Assess the morphology of the erythrocytes.
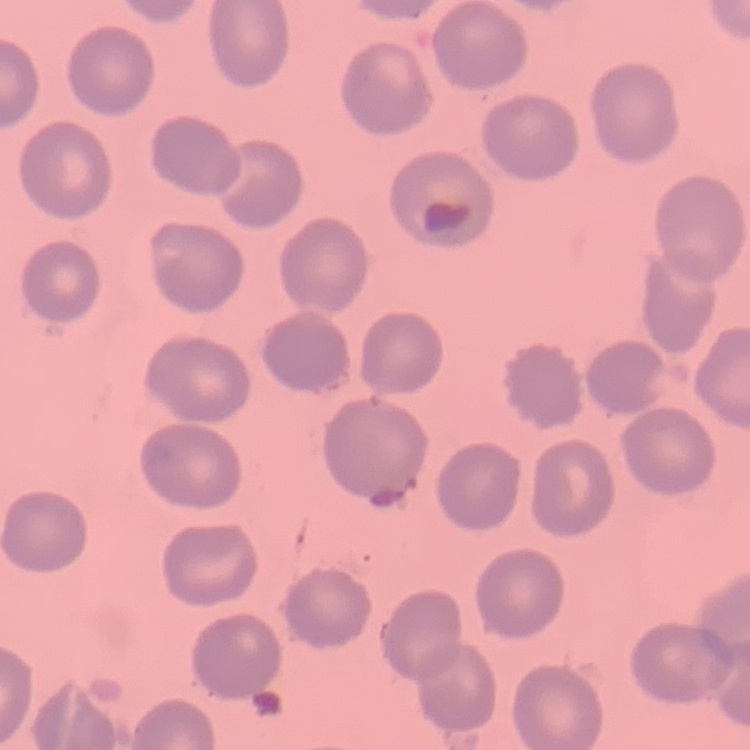

They show no rouleaux formation.

stain = Field's or Giemsa
preparation = thin peripheral smear
image type = one tile cut from a larger photomicrograph